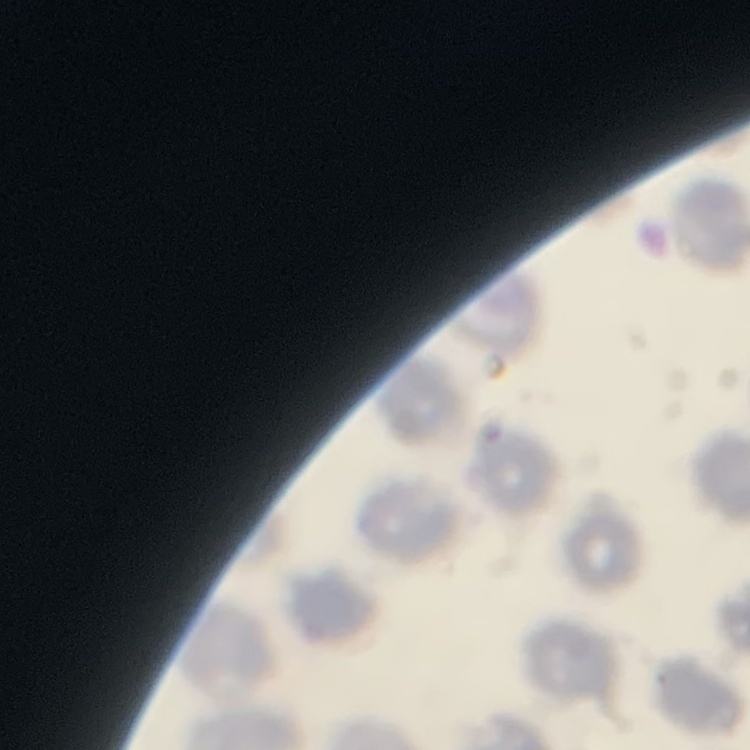

Summary:
  - Erythrocyte morphology: no rouleaux formation
  - Image type: square crop of a larger photomicrograph
  - Preparation: thin blood smear
  - Stain: Field's or Giemsa